Comment on the morphology of the erythrocytes.
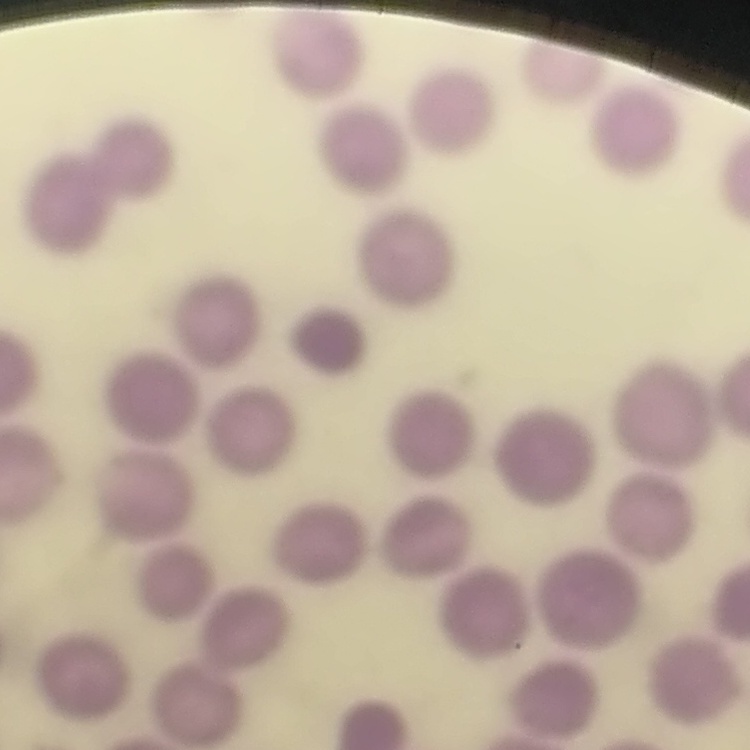
They show no rouleaux formation.

Thin blood film. Stained with either Field's or Giemsa. Square crop of a larger photomicrograph.